Locate every uninfected red blood cell.
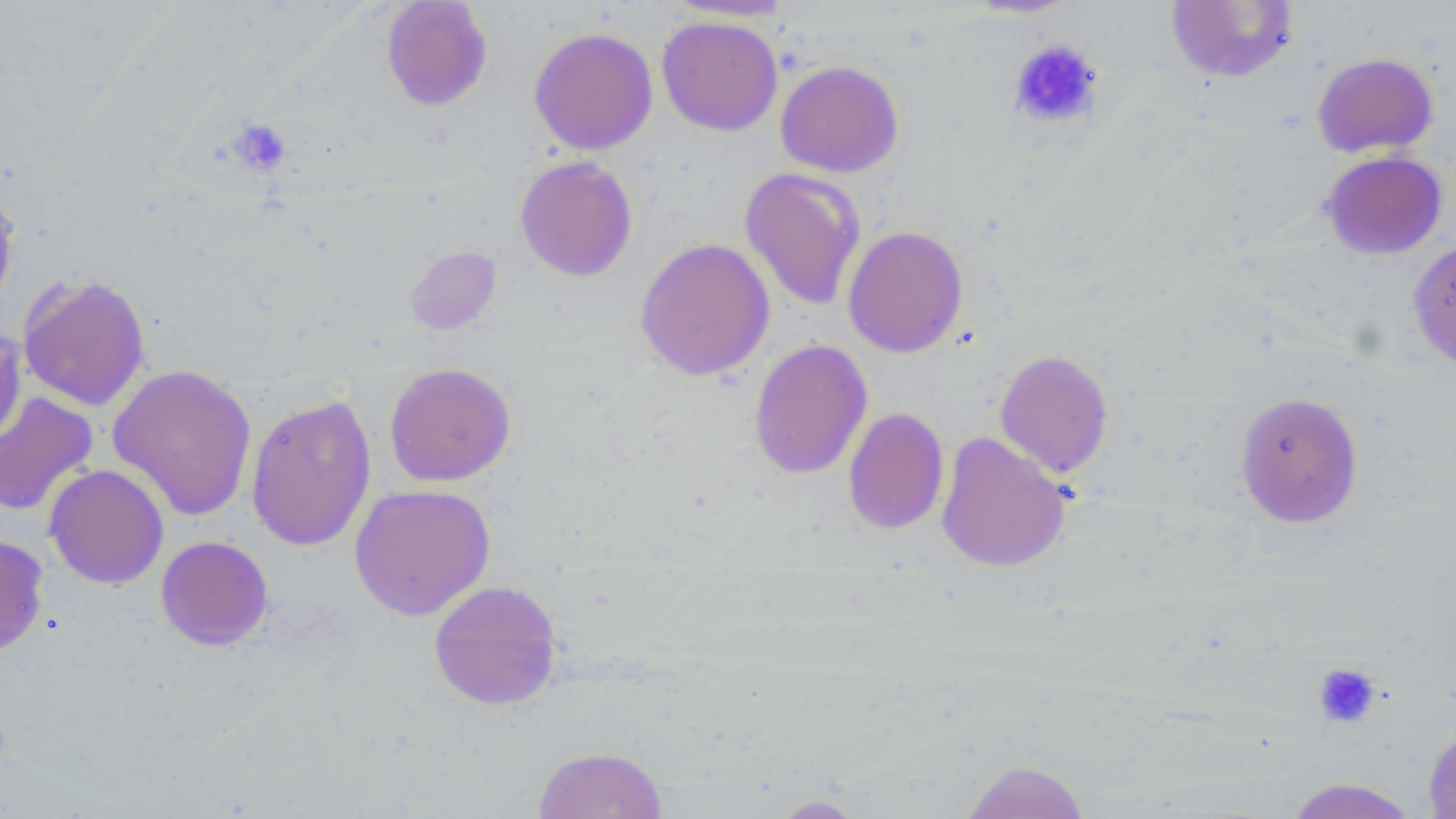
Approximate bounding boxes as (x1,y1)-(x2,y2) corner pairs in pixels.
Uninfected red blood cells: (380,0)-(493,111), (663,0)-(797,21), (1166,1)-(1299,84), (656,15)-(783,136), (528,26)-(658,155), (1311,52)-(1438,159), (775,59)-(904,178), (1319,150)-(1448,260), (514,155)-(638,282), (739,167)-(867,311), (0,178)-(21,318), (842,225)-(968,358), (635,237)-(775,382), (1407,237)-(1456,373), (405,246)-(501,334), (17,273)-(151,411), (0,326)-(26,451), (749,339)-(872,480), (994,349)-(1114,478), (383,363)-(516,487), (107,364)-(257,521), (1234,390)-(1364,528), (0,391)-(99,518), (245,393)-(377,551), (843,407)-(949,535), (935,431)-(1071,573), (44,464)-(169,589), (349,483)-(495,620), (0,534)-(49,658), (155,535)-(273,651), (429,579)-(562,710), (1422,722)-(1456,819), (531,745)-(668,819), (959,760)-(1091,818), (1283,778)-(1421,819), (766,794)-(873,818).

Platelet locations: (1008,39)-(1105,130), (228,117)-(293,177), (1313,663)-(1382,729). Slide-level diagnosis: no evidence of blood parasites. Image is 1456×819 pixels. Light microscopy. Single field of view. 1000x magnification. May-Grünwald-Giemsa stain. Thin blood smear.